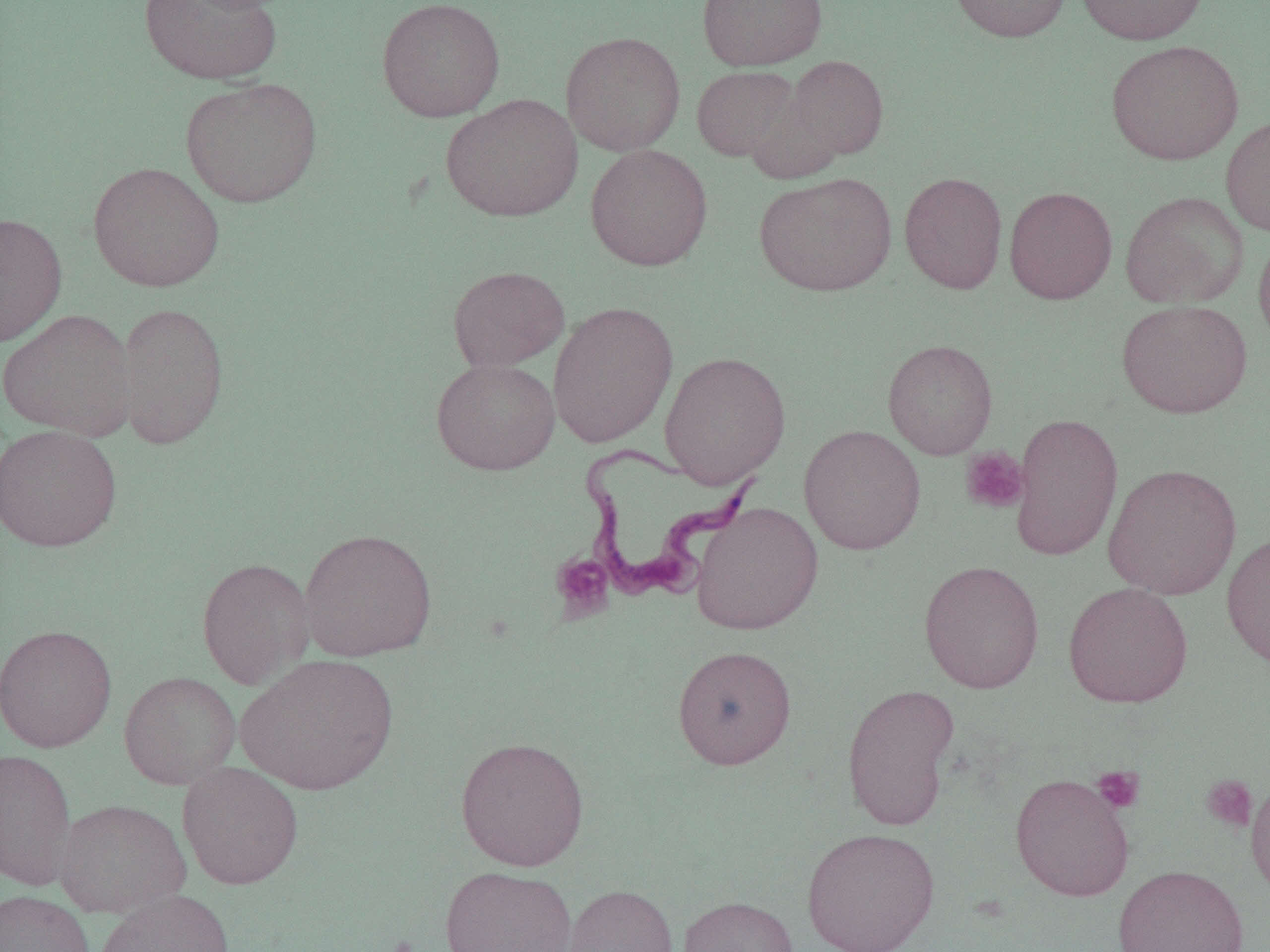 Approximate bounding boxes as (x1, y1, x2, y2) in pixels. Platelet locations: (960, 447, 1029, 514), (550, 553, 614, 621), (1092, 765, 1145, 814), (1201, 774, 1257, 832). Trypanosoma brucei locations: (576, 443, 763, 606). Uninfected red blood cell locations: (139, 0, 282, 84), (376, 0, 505, 122), (697, 0, 828, 71), (947, 0, 1073, 42), (1075, 0, 1208, 45), (561, 31, 686, 156), (1106, 39, 1244, 165), (785, 55, 889, 159), (691, 66, 798, 162), (180, 77, 323, 208), (745, 91, 846, 185), (441, 93, 583, 222), (1221, 115, 1270, 237), (584, 144, 713, 271), (88, 161, 225, 292), (754, 172, 897, 296), (899, 172, 1008, 294), (1004, 186, 1117, 304), (1120, 191, 1249, 309), (0, 212, 67, 347), (1254, 230, 1270, 352), (447, 265, 570, 372), (1116, 299, 1252, 418), (116, 301, 229, 450), (547, 301, 678, 448), (0, 309, 137, 440), (882, 339, 998, 460), (660, 350, 791, 489), (431, 358, 560, 475), (1009, 412, 1123, 562), (0, 424, 122, 552), (798, 424, 926, 555), (1103, 463, 1241, 600), (691, 501, 823, 635), (298, 527, 438, 661), (1221, 532, 1270, 671), (196, 557, 315, 689), (918, 560, 1045, 693), (1063, 582, 1193, 708), (0, 624, 117, 752), (672, 645, 797, 769), (236, 653, 399, 795), (119, 671, 241, 790), (842, 682, 960, 831), (455, 735, 590, 872), (0, 748, 78, 891), (177, 761, 304, 889), (1011, 773, 1135, 901), (1246, 774, 1270, 901), (54, 799, 191, 918), (800, 828, 941, 952), (1113, 864, 1250, 952), (439, 865, 577, 952), (560, 884, 678, 952), (0, 889, 94, 952), (95, 889, 236, 952), (677, 895, 799, 952). Slide-level diagnosis: Trypanosoma brucei. 1000x magnification. Light microscopy. Image is 1270×952 pixels. One field of a larger specimen. Thin blood film.